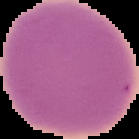
Summary:
  - Malaria status: uninfected
  - Image size: 139×139 pixels
  - Image type: cell region segmented out of the field of view; surrounding area masked to black
  - Preparation: thin blood film